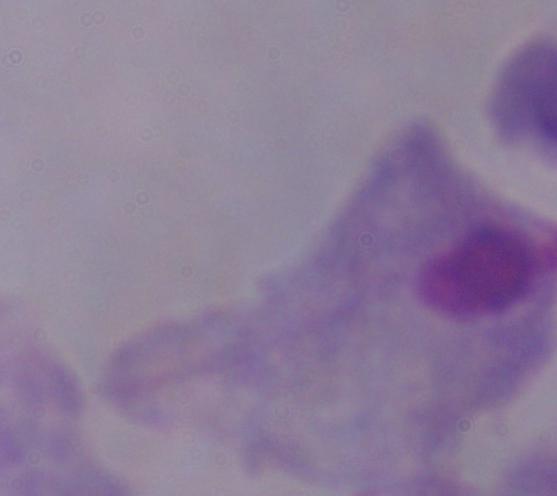 A trichomonad is seen. 1000x magnification. Photomicrograph.